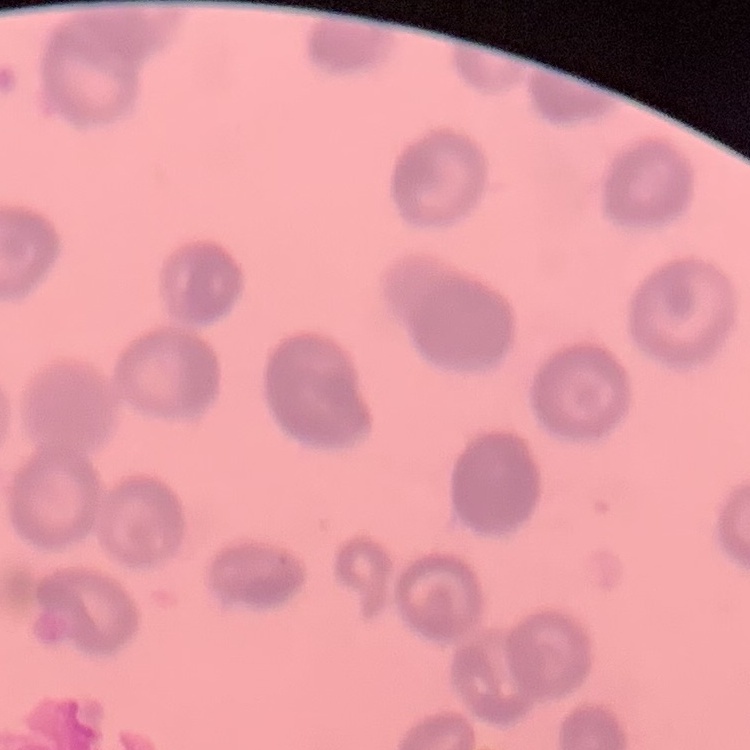

red blood cell morphology = rouleaux formation
image type = square crop of a larger photomicrograph
stain = Field's or Giemsa
preparation = thin blood film